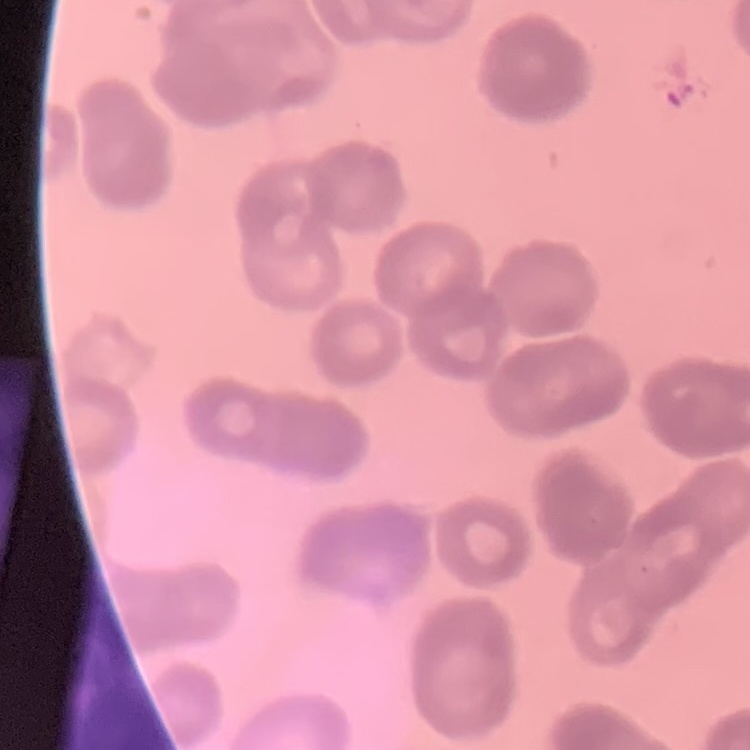

Summary:
  - Erythrocyte morphology: rouleaux formation
  - Image type: one tile cut from a larger photomicrograph
  - Preparation: thin peripheral smear
  - Stain: Field's or Giemsa